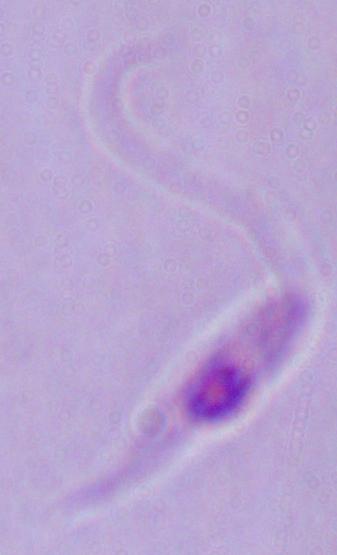

Summary:
  - Identification: Leishmania
  - Modality: photomicrograph
  - Magnification: 1000x